Name the blood parasite species.
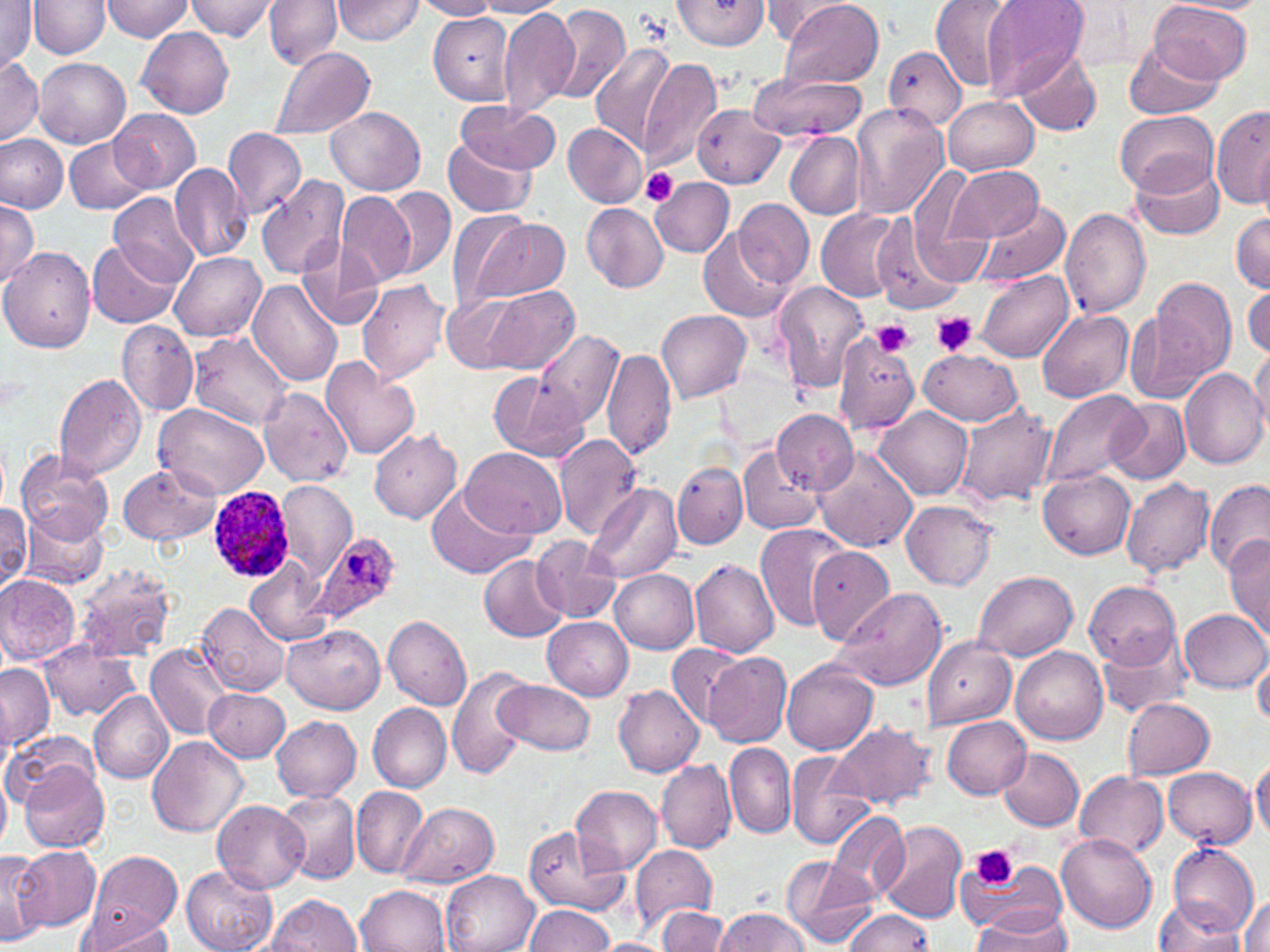
Plasmodium ovale.

Approximate bounding boxes as named x1/y1/x2/y2 corners in pixels. Plasmodium ovale-infected red blood cell locations: (x1=206, y1=486, x2=296, y2=582), (x1=309, y1=530, x2=400, y2=628). Platelet locations: (x1=641, y1=169, x2=679, y2=205), (x1=930, y1=311, x2=980, y2=357), (x1=873, y1=319, x2=915, y2=357), (x1=970, y1=843, x2=1018, y2=890). Uninfected red blood cell locations: (x1=0, y1=0, x2=38, y2=69), (x1=99, y1=0, x2=194, y2=41), (x1=187, y1=0, x2=280, y2=41), (x1=264, y1=0, x2=342, y2=69), (x1=333, y1=0, x2=426, y2=44), (x1=412, y1=0, x2=502, y2=20), (x1=670, y1=0, x2=773, y2=52), (x1=759, y1=0, x2=847, y2=42), (x1=780, y1=0, x2=886, y2=89), (x1=930, y1=0, x2=1018, y2=92), (x1=979, y1=0, x2=1090, y2=102), (x1=1170, y1=0, x2=1264, y2=14), (x1=29, y1=1, x2=109, y2=59), (x1=473, y1=1, x2=569, y2=17), (x1=1149, y1=1, x2=1253, y2=83), (x1=1056, y1=2, x2=1155, y2=77), (x1=546, y1=5, x2=630, y2=104), (x1=497, y1=6, x2=579, y2=114), (x1=429, y1=11, x2=518, y2=100), (x1=138, y1=26, x2=235, y2=117), (x1=1123, y1=38, x2=1222, y2=120), (x1=591, y1=42, x2=676, y2=149), (x1=884, y1=45, x2=966, y2=133), (x1=268, y1=48, x2=374, y2=141), (x1=1014, y1=49, x2=1102, y2=136), (x1=0, y1=57, x2=43, y2=146), (x1=34, y1=57, x2=131, y2=148), (x1=638, y1=57, x2=722, y2=172), (x1=749, y1=73, x2=866, y2=142), (x1=943, y1=96, x2=1038, y2=175), (x1=453, y1=101, x2=559, y2=175), (x1=692, y1=102, x2=785, y2=189), (x1=851, y1=104, x2=948, y2=220), (x1=1212, y1=105, x2=1270, y2=208), (x1=326, y1=107, x2=425, y2=195), (x1=109, y1=108, x2=200, y2=192), (x1=1116, y1=110, x2=1217, y2=194), (x1=563, y1=123, x2=647, y2=208), (x1=222, y1=127, x2=306, y2=220), (x1=785, y1=132, x2=865, y2=220), (x1=0, y1=133, x2=68, y2=214), (x1=442, y1=133, x2=541, y2=218), (x1=65, y1=137, x2=150, y2=214), (x1=1131, y1=157, x2=1225, y2=241), (x1=170, y1=163, x2=254, y2=261), (x1=945, y1=164, x2=1044, y2=241), (x1=910, y1=165, x2=976, y2=255), (x1=256, y1=176, x2=348, y2=280), (x1=650, y1=177, x2=734, y2=257), (x1=380, y1=186, x2=456, y2=281), (x1=110, y1=192, x2=199, y2=285), (x1=336, y1=192, x2=415, y2=286), (x1=734, y1=198, x2=814, y2=288), (x1=0, y1=201, x2=40, y2=288), (x1=974, y1=201, x2=1071, y2=285), (x1=582, y1=202, x2=668, y2=291), (x1=443, y1=206, x2=529, y2=312), (x1=816, y1=208, x2=902, y2=301), (x1=1061, y1=208, x2=1151, y2=317), (x1=1231, y1=210, x2=1270, y2=294), (x1=466, y1=217, x2=569, y2=303), (x1=872, y1=217, x2=965, y2=313), (x1=701, y1=227, x2=793, y2=323), (x1=298, y1=238, x2=385, y2=331), (x1=87, y1=239, x2=180, y2=328), (x1=0, y1=247, x2=95, y2=353), (x1=170, y1=252, x2=265, y2=339), (x1=976, y1=269, x2=1074, y2=361), (x1=1152, y1=278, x2=1238, y2=382), (x1=356, y1=280, x2=450, y2=385), (x1=247, y1=281, x2=343, y2=388), (x1=771, y1=281, x2=870, y2=393), (x1=485, y1=283, x2=579, y2=374), (x1=1245, y1=283, x2=1270, y2=363), (x1=444, y1=294, x2=524, y2=374), (x1=657, y1=309, x2=752, y2=401), (x1=1037, y1=309, x2=1134, y2=402), (x1=1124, y1=312, x2=1211, y2=405), (x1=117, y1=320, x2=199, y2=417), (x1=536, y1=331, x2=624, y2=431), (x1=188, y1=332, x2=294, y2=430), (x1=833, y1=338, x2=919, y2=434), (x1=602, y1=347, x2=676, y2=462), (x1=1249, y1=347, x2=1270, y2=436), (x1=920, y1=348, x2=1023, y2=426), (x1=320, y1=357, x2=422, y2=461), (x1=1178, y1=369, x2=1270, y2=469), (x1=488, y1=371, x2=588, y2=463), (x1=54, y1=373, x2=148, y2=481), (x1=261, y1=388, x2=351, y2=484), (x1=1043, y1=389, x2=1146, y2=492), (x1=1106, y1=396, x2=1191, y2=485), (x1=954, y1=403, x2=1058, y2=507), (x1=156, y1=404, x2=270, y2=499), (x1=874, y1=406, x2=971, y2=501), (x1=772, y1=409, x2=857, y2=492), (x1=369, y1=429, x2=463, y2=524), (x1=554, y1=433, x2=643, y2=539), (x1=811, y1=443, x2=919, y2=552), (x1=738, y1=446, x2=823, y2=535), (x1=460, y1=447, x2=568, y2=541), (x1=16, y1=450, x2=114, y2=546), (x1=673, y1=461, x2=747, y2=548), (x1=117, y1=464, x2=220, y2=546), (x1=1039, y1=470, x2=1135, y2=559), (x1=1121, y1=477, x2=1215, y2=580), (x1=277, y1=480, x2=356, y2=576), (x1=1202, y1=481, x2=1268, y2=578), (x1=584, y1=484, x2=681, y2=583), (x1=428, y1=485, x2=529, y2=580), (x1=902, y1=500, x2=997, y2=591), (x1=0, y1=503, x2=32, y2=592), (x1=18, y1=507, x2=110, y2=591), (x1=757, y1=523, x2=853, y2=631), (x1=1224, y1=535, x2=1270, y2=638), (x1=532, y1=536, x2=620, y2=623), (x1=806, y1=547, x2=896, y2=647), (x1=246, y1=554, x2=333, y2=645), (x1=480, y1=555, x2=570, y2=641), (x1=689, y1=559, x2=780, y2=657), (x1=75, y1=564, x2=176, y2=662), (x1=610, y1=569, x2=700, y2=653), (x1=973, y1=569, x2=1078, y2=658), (x1=0, y1=574, x2=80, y2=665), (x1=1085, y1=580, x2=1181, y2=668), (x1=832, y1=586, x2=947, y2=691), (x1=197, y1=602, x2=289, y2=696), (x1=1180, y1=610, x2=1268, y2=692), (x1=383, y1=616, x2=472, y2=710), (x1=542, y1=616, x2=635, y2=700), (x1=283, y1=626, x2=385, y2=714), (x1=1096, y1=628, x2=1195, y2=718), (x1=923, y1=638, x2=1015, y2=728), (x1=42, y1=640, x2=139, y2=720), (x1=148, y1=643, x2=231, y2=739), (x1=665, y1=643, x2=744, y2=727), (x1=1010, y1=646, x2=1107, y2=744), (x1=1252, y1=649, x2=1270, y2=728), (x1=704, y1=651, x2=791, y2=748), (x1=783, y1=660, x2=878, y2=754), (x1=1, y1=663, x2=53, y2=751), (x1=447, y1=663, x2=530, y2=782), (x1=497, y1=680, x2=596, y2=756), (x1=612, y1=685, x2=704, y2=778), (x1=205, y1=688, x2=289, y2=761), (x1=89, y1=691, x2=174, y2=783), (x1=1117, y1=696, x2=1228, y2=845), (x1=1123, y1=699, x2=1215, y2=779), (x1=368, y1=702, x2=451, y2=793), (x1=361, y1=705, x2=440, y2=877), (x1=270, y1=716, x2=361, y2=801), (x1=942, y1=716, x2=1032, y2=799), (x1=833, y1=721, x2=938, y2=810), (x1=6, y1=729, x2=103, y2=807), (x1=147, y1=735, x2=247, y2=837), (x1=724, y1=742, x2=795, y2=840), (x1=998, y1=747, x2=1084, y2=832), (x1=785, y1=750, x2=874, y2=850), (x1=656, y1=758, x2=736, y2=853), (x1=1250, y1=758, x2=1270, y2=841), (x1=19, y1=761, x2=109, y2=854), (x1=1163, y1=765, x2=1256, y2=848), (x1=1074, y1=770, x2=1168, y2=858), (x1=0, y1=776, x2=10, y2=853), (x1=570, y1=784, x2=663, y2=874), (x1=350, y1=786, x2=430, y2=879), (x1=277, y1=792, x2=359, y2=886), (x1=213, y1=799, x2=309, y2=893), (x1=396, y1=802, x2=499, y2=888), (x1=824, y1=809, x2=911, y2=904), (x1=877, y1=818, x2=969, y2=925), (x1=521, y1=825, x2=628, y2=917), (x1=1056, y1=833, x2=1158, y2=934), (x1=1166, y1=840, x2=1259, y2=936), (x1=14, y1=845, x2=100, y2=931), (x1=629, y1=845, x2=717, y2=931), (x1=0, y1=849, x2=47, y2=944), (x1=84, y1=850, x2=182, y2=945), (x1=954, y1=854, x2=1067, y2=938), (x1=780, y1=855, x2=879, y2=948), (x1=182, y1=865, x2=277, y2=952), (x1=440, y1=869, x2=538, y2=952), (x1=356, y1=884, x2=451, y2=952), (x1=265, y1=893, x2=363, y2=951), (x1=1238, y1=893, x2=1270, y2=952), (x1=1151, y1=897, x2=1246, y2=952), (x1=655, y1=904, x2=729, y2=951), (x1=970, y1=904, x2=1073, y2=951), (x1=522, y1=905, x2=616, y2=952), (x1=843, y1=908, x2=935, y2=952), (x1=716, y1=909, x2=811, y2=952), (x1=79, y1=911, x2=175, y2=951), (x1=595, y1=938, x2=670, y2=952). One field of a larger specimen. Image is 1270×952 pixels. Optical microscopy. May-Grünwald-Giemsa-stained preparation. Thin blood film. 1000x magnification.